State which parasite is depicted.
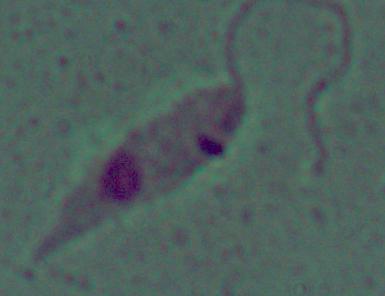

Leishmania.

magnification = 1000x
modality = photomicrograph